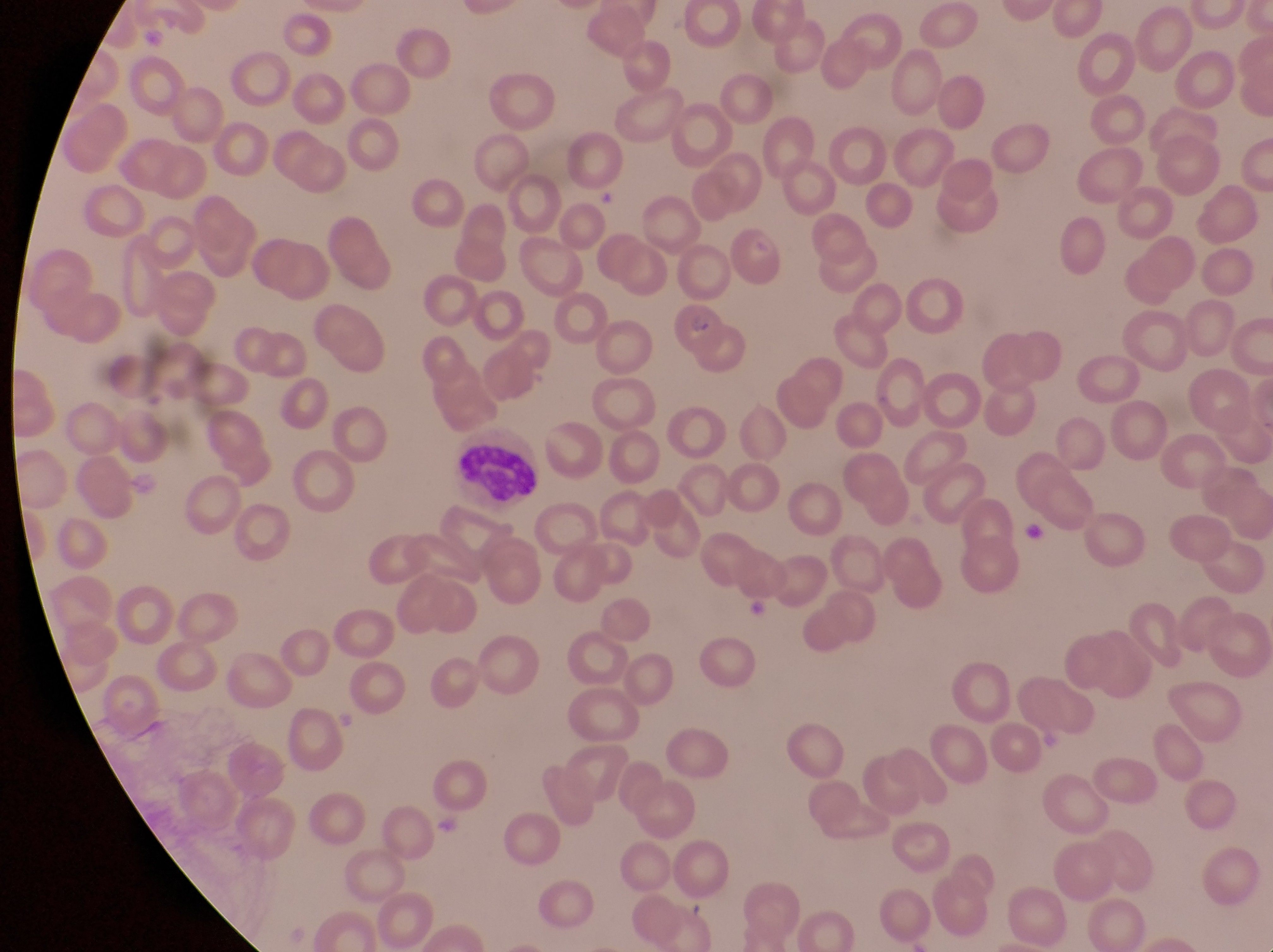

Approximate bounding boxes as (left, top, right, bottom) in pixels. Leukocyte locations: (454, 445, 542, 507). Parasitised red blood cell locations: (667, 299, 730, 361). Sample from Uganda. Thin blood film. Photographed through the eyepiece of an Olympus CX-23 microscope with a smartphone camera. Image is 1273×952 pixels. Magnification of 1000x. One field of view.